Locate every Plasmodium falciparum-infected red blood cell.
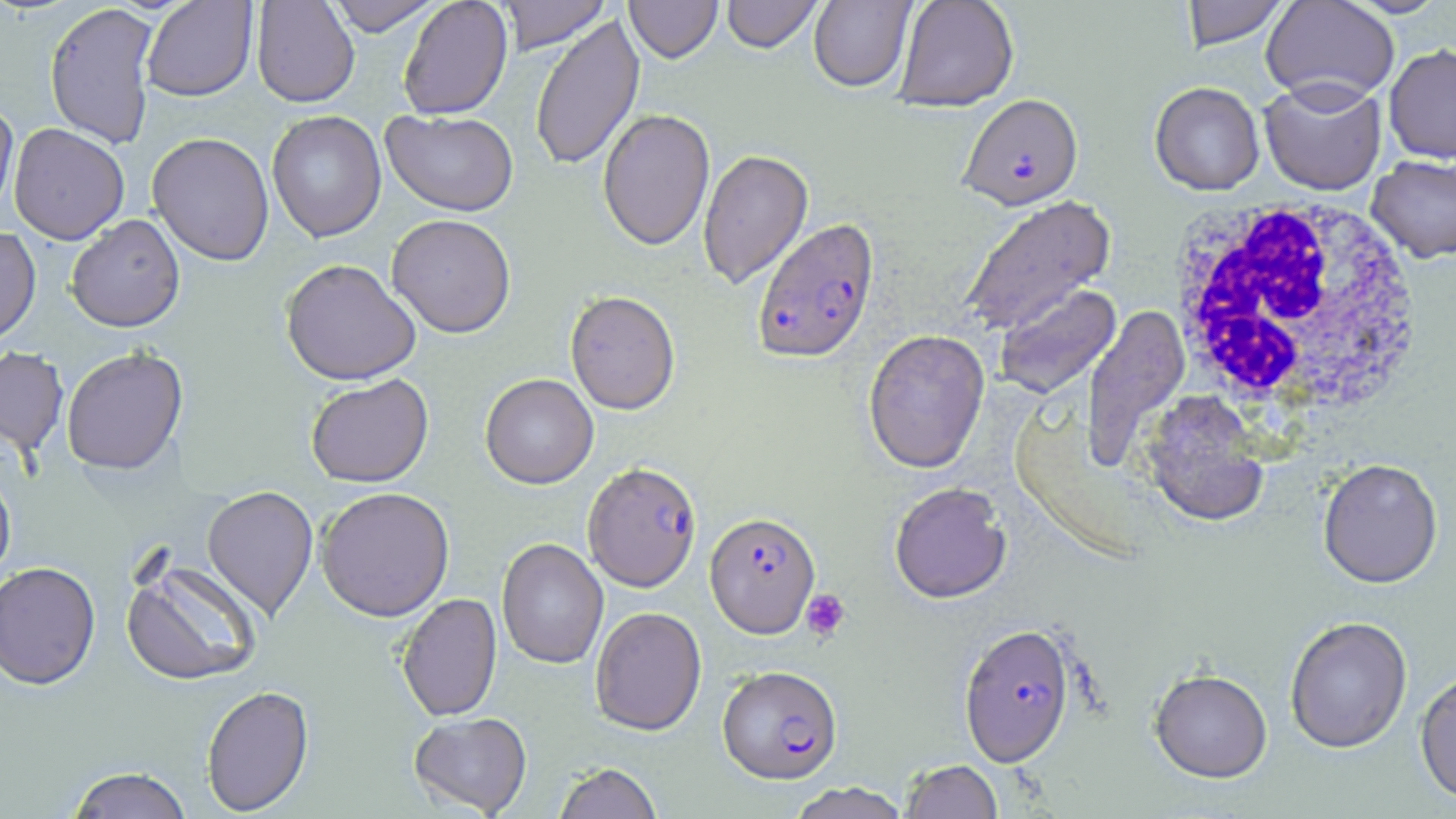

Approximate bounding boxes as (x1, y1, x2, y2) in pixels.
Plasmodium falciparum-infected red blood cells: (959, 93, 1083, 210), (751, 216, 880, 364), (582, 461, 702, 592), (704, 512, 820, 638), (958, 623, 1076, 767), (718, 664, 842, 783).

{
  "slide_level_diagnosis": "Plasmodium falciparum",
  "magnification": "1000x",
  "white_blood_cell_locations": "approximate bounding boxes as (x1, y1, x2, y2) in pixels: (1165, 195, 1427, 421)",
  "preparation": "thin blood smear",
  "stain": "May-Grünwald-Giemsa",
  "image_size": "1456×819 pixels",
  "platelet_locations": "approximate bounding boxes as (x1, y1, x2, y2) in pixels: (801, 589, 851, 641)",
  "uninfected_red_blood_cell_locations": "approximate bounding boxes as (x1, y1, x2, y2) in pixels: (251, 0, 359, 107), (325, 0, 442, 36), (398, 0, 512, 119), (496, 0, 610, 54), (625, 0, 723, 62), (722, 0, 823, 53), (808, 0, 917, 93), (893, 0, 1019, 111), (1179, 0, 1292, 50), (1261, 0, 1399, 106), (141, 1, 258, 101), (44, 2, 159, 149), (529, 14, 645, 172), (1384, 43, 1456, 164), (1259, 79, 1386, 196), (1149, 81, 1265, 195), (0, 97, 19, 224), (598, 108, 715, 250), (381, 109, 519, 216), (267, 110, 386, 243), (9, 123, 129, 244), (147, 132, 275, 266), (697, 148, 814, 290), (1366, 154, 1456, 263), (959, 195, 1116, 335), (387, 213, 516, 337), (66, 214, 185, 332), (0, 227, 41, 346), (280, 258, 421, 385), (995, 283, 1121, 400), (565, 290, 681, 414), (1082, 303, 1190, 473), (862, 329, 990, 474), (0, 346, 69, 457), (61, 346, 188, 475), (480, 373, 598, 489), (305, 374, 434, 487), (1139, 390, 1272, 527), (1318, 458, 1442, 588), (0, 465, 16, 585), (889, 481, 1012, 603), (202, 484, 318, 621), (316, 486, 455, 621), (497, 538, 609, 669), (120, 557, 263, 687), (0, 560, 101, 690), (397, 592, 501, 721), (590, 606, 707, 735), (1284, 615, 1413, 753), (1414, 667, 1456, 806), (1149, 668, 1273, 782), (201, 685, 314, 816), (408, 711, 532, 817), (899, 759, 1004, 819), (553, 762, 663, 819), (66, 766, 193, 818), (785, 782, 912, 819)",
  "modality": "optical microscopy",
  "field_of_view": "one of a larger specimen"
}